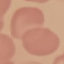
Malaria status: uninfected. Photographed with a smartphone camera at the microscope eyepiece. Thin smear of blood. Giemsa-stained preparation. Automatically extracted cell patch, resized to 64 × 64 pixels.